Give the position of every Plasmodium parasite.
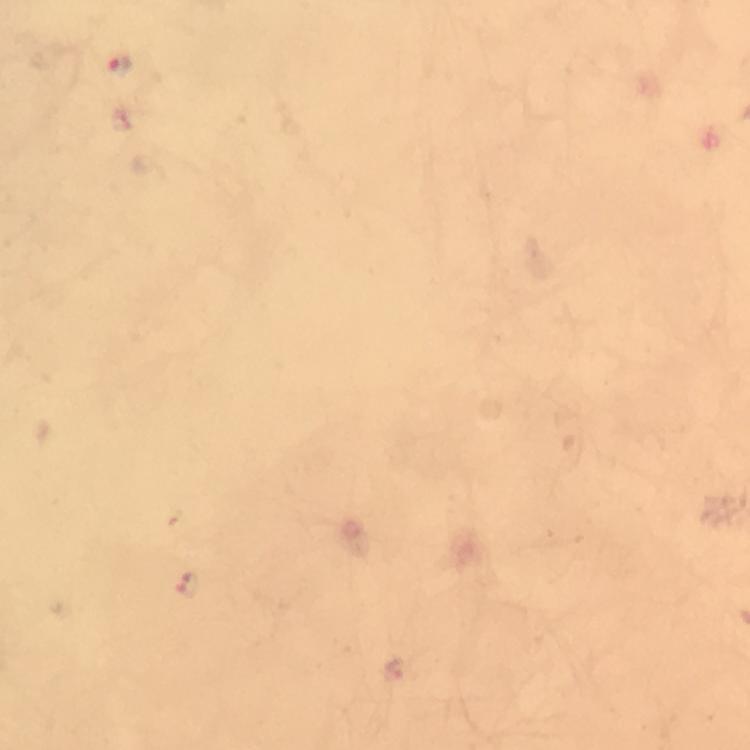

Approximate centers as (x, y) in pixels.
Plasmodium parasites: (119, 66), (189, 584).

100x magnification. Giemsa stain. Thick smear. From a malaria diagnostic workup. Image is 750×750 pixels. Smartphone photograph taken through a microscope. Immersion oil was used. Cropped region of a single field of view.